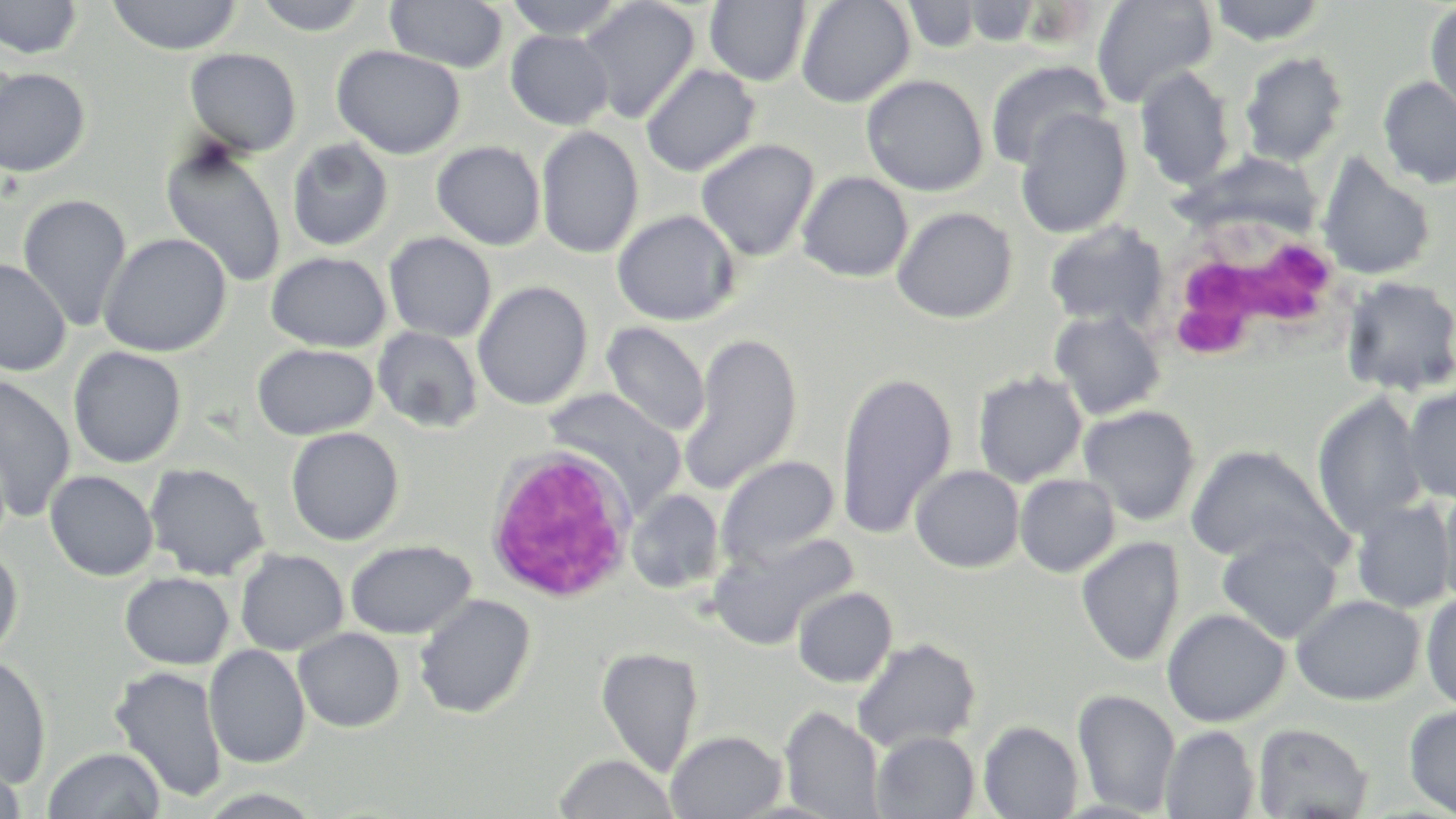

Summary:
  - Coordinate format: approximate bounding boxes as named x1/y1/x2/y2 corners in pixels
  - Uninfected red blood cell locations: (x1=0, y1=0, x2=83, y2=60), (x1=107, y1=0, x2=242, y2=55), (x1=252, y1=0, x2=373, y2=36), (x1=385, y1=0, x2=508, y2=72), (x1=503, y1=0, x2=628, y2=40), (x1=578, y1=0, x2=700, y2=123), (x1=796, y1=0, x2=915, y2=108), (x1=1091, y1=0, x2=1217, y2=108), (x1=1207, y1=0, x2=1331, y2=46), (x1=705, y1=1, x2=813, y2=86), (x1=901, y1=1, x2=983, y2=53), (x1=959, y1=1, x2=1044, y2=47), (x1=1424, y1=2, x2=1456, y2=120), (x1=506, y1=30, x2=614, y2=130), (x1=332, y1=45, x2=466, y2=159), (x1=185, y1=48, x2=302, y2=156), (x1=1239, y1=51, x2=1348, y2=167), (x1=0, y1=57, x2=19, y2=162), (x1=984, y1=60, x2=1110, y2=171), (x1=641, y1=63, x2=760, y2=177), (x1=0, y1=66, x2=91, y2=178), (x1=1134, y1=67, x2=1237, y2=191), (x1=861, y1=74, x2=988, y2=196), (x1=1378, y1=76, x2=1456, y2=189), (x1=1015, y1=109, x2=1132, y2=238), (x1=536, y1=126, x2=644, y2=259), (x1=286, y1=138, x2=394, y2=251), (x1=695, y1=138, x2=819, y2=262), (x1=160, y1=139, x2=287, y2=288), (x1=432, y1=141, x2=546, y2=250), (x1=1316, y1=154, x2=1436, y2=281), (x1=796, y1=171, x2=913, y2=283), (x1=18, y1=193, x2=132, y2=332), (x1=892, y1=206, x2=1018, y2=323), (x1=612, y1=210, x2=740, y2=326), (x1=1043, y1=220, x2=1169, y2=331), (x1=98, y1=232, x2=232, y2=357), (x1=383, y1=232, x2=497, y2=343), (x1=266, y1=251, x2=391, y2=352), (x1=0, y1=259, x2=71, y2=376), (x1=1338, y1=274, x2=1456, y2=397), (x1=473, y1=281, x2=594, y2=410), (x1=1049, y1=310, x2=1166, y2=420), (x1=600, y1=321, x2=711, y2=437), (x1=372, y1=326, x2=483, y2=434), (x1=679, y1=332, x2=803, y2=495), (x1=252, y1=343, x2=379, y2=440), (x1=68, y1=346, x2=187, y2=469), (x1=835, y1=369, x2=956, y2=541), (x1=972, y1=370, x2=1088, y2=487), (x1=0, y1=375, x2=76, y2=522), (x1=1401, y1=386, x2=1456, y2=504), (x1=542, y1=387, x2=687, y2=512), (x1=1311, y1=393, x2=1430, y2=538), (x1=1078, y1=405, x2=1201, y2=526), (x1=285, y1=426, x2=404, y2=546), (x1=1186, y1=444, x2=1341, y2=566), (x1=715, y1=455, x2=840, y2=569), (x1=144, y1=462, x2=270, y2=580), (x1=910, y1=465, x2=1024, y2=573), (x1=45, y1=470, x2=159, y2=580), (x1=1014, y1=474, x2=1120, y2=577), (x1=1438, y1=485, x2=1456, y2=610), (x1=626, y1=489, x2=724, y2=594), (x1=1350, y1=499, x2=1454, y2=614), (x1=711, y1=530, x2=858, y2=649), (x1=1216, y1=531, x2=1342, y2=644), (x1=1076, y1=536, x2=1185, y2=667), (x1=345, y1=539, x2=476, y2=640), (x1=0, y1=548, x2=23, y2=663), (x1=235, y1=548, x2=349, y2=655), (x1=120, y1=572, x2=234, y2=669), (x1=792, y1=586, x2=897, y2=688), (x1=1420, y1=591, x2=1456, y2=712), (x1=414, y1=593, x2=536, y2=718), (x1=1292, y1=594, x2=1425, y2=706), (x1=1162, y1=607, x2=1290, y2=727), (x1=293, y1=627, x2=405, y2=732), (x1=851, y1=637, x2=982, y2=754), (x1=204, y1=644, x2=310, y2=769), (x1=596, y1=646, x2=704, y2=778), (x1=0, y1=653, x2=51, y2=788), (x1=109, y1=664, x2=227, y2=803), (x1=1073, y1=689, x2=1180, y2=815), (x1=1404, y1=704, x2=1456, y2=817), (x1=780, y1=706, x2=885, y2=819), (x1=979, y1=721, x2=1083, y2=818), (x1=1252, y1=723, x2=1373, y2=819), (x1=1160, y1=725, x2=1260, y2=818), (x1=666, y1=729, x2=787, y2=818), (x1=872, y1=730, x2=980, y2=818), (x1=42, y1=746, x2=166, y2=819), (x1=554, y1=753, x2=678, y2=818), (x1=0, y1=756, x2=27, y2=819)
  - White blood cell locations: (x1=1154, y1=213, x2=1342, y2=364), (x1=484, y1=446, x2=638, y2=603)
  - Slide-level diagnosis: no evidence of blood parasites
  - Field of view: single
  - Modality: light microscopy
  - Image size: 1456×819 pixels
  - Stain: May-Grünwald-Giemsa
  - Magnification: 1000x
  - Preparation: thin blood smear